Report the malaria status of this cell.
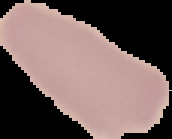

Uninfected.

preparation = thin blood film
image size = 172×139 pixels
image type = segmented cell region on a black background